Assess the morphology of the red blood cells.
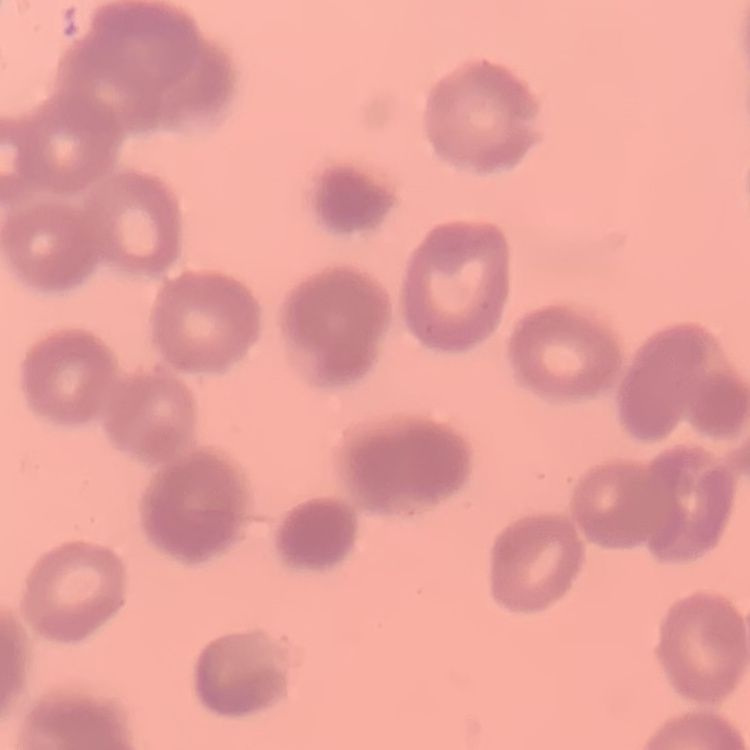

Rouleaux formation.

Stained with either Field's or Giemsa. Thin blood smear. One tile cut from a larger photomicrograph.